Classify this cell by malaria status.
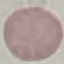
It is uninfected.

Summary:
  - Preparation: thin smear
  - Stain: Giemsa
  - Image type: automatically extracted cell patch, resized to 64 × 64 pixels
  - Capture: smartphone through the microscope eyepiece